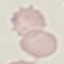

Summary:
  - Malaria status: uninfected
  - Capture: smartphone through the microscope eyepiece
  - Preparation: thin blood film
  - Stain: Giemsa
  - Image type: cell patch, automatically extracted from a larger field of view and resized to 64 × 64 pixels